State which parasite is depicted.
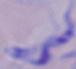
A trypanosome.

1000x magnification. Photomicrograph.